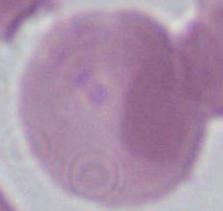

{
  "magnification": "1000x",
  "modality": "micrograph",
  "identification": "red blood cell"
}